Identify the cell.
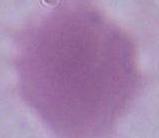

This is an erythrocyte.

{
  "modality": "photomicrograph",
  "magnification": "1000x"
}